Locate every blood parasite and identify its species.
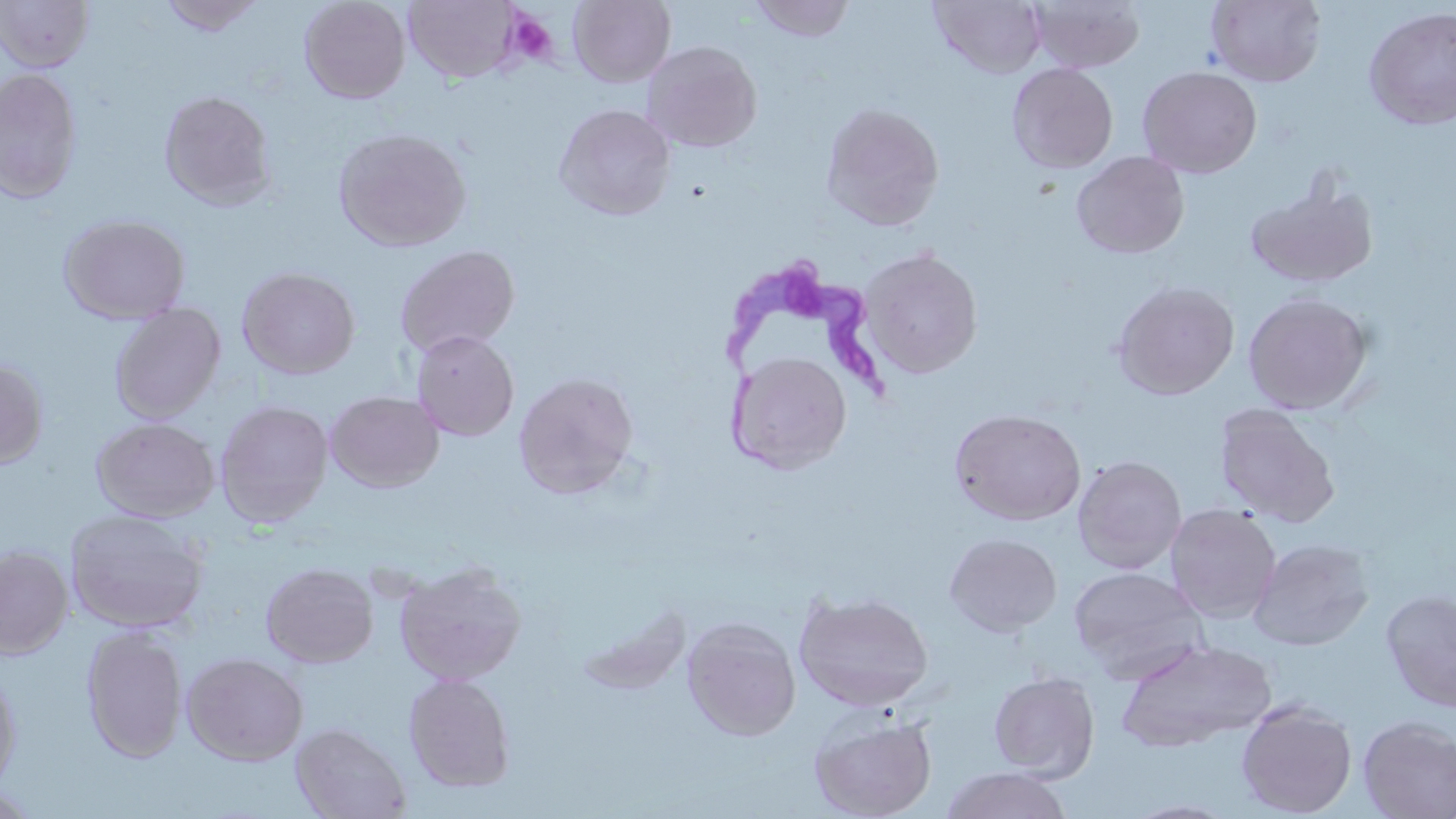

Approximate bounding boxes as (x1,y1)-(x2,y2) corner pairs in pixels.
Trypanosoma brucei: (723,255)-(890,478).
No Plasmodium falciparum, Plasmodium ovale, Plasmodium malariae, Plasmodium vivax, or Babesia divergens observed.

Platelet locations: (515,15)-(560,68). Uninfected red blood cell locations: (0,0)-(94,72), (157,0)-(267,37), (299,0)-(410,104), (568,0)-(675,87), (747,0)-(855,42), (1206,0)-(1326,87), (403,1)-(521,83), (929,1)-(1046,78), (1028,1)-(1145,74), (1363,6)-(1456,129), (642,40)-(763,153), (1007,63)-(1118,174), (1137,66)-(1262,178), (0,68)-(82,204), (158,90)-(277,209), (553,103)-(676,221), (821,103)-(944,231), (334,127)-(471,252), (1071,150)-(1190,259), (1244,177)-(1379,288), (58,213)-(192,325), (395,244)-(520,358), (859,247)-(983,378), (236,266)-(361,380), (1112,280)-(1240,399), (1243,291)-(1373,414), (109,303)-(226,424), (410,330)-(519,442), (728,351)-(852,474), (0,356)-(48,470), (513,372)-(639,499), (324,390)-(444,493), (215,400)-(334,528), (1214,404)-(1340,526), (949,409)-(1086,525), (91,417)-(220,522), (1072,454)-(1188,575), (1165,503)-(1282,623), (65,508)-(208,634), (945,533)-(1062,636), (1249,537)-(1375,651), (0,545)-(74,658), (394,560)-(527,686), (261,562)-(378,668), (1069,566)-(1208,680), (1380,588)-(1456,714), (794,589)-(934,711), (681,616)-(802,741), (81,625)-(188,762), (1114,638)-(1278,752), (181,651)-(309,765), (0,664)-(22,795), (988,670)-(1099,781), (403,672)-(516,793), (1236,699)-(1358,817), (809,711)-(937,819), (1357,716)-(1456,819), (290,721)-(412,819), (940,767)-(1073,819), (0,785)-(43,819). Slide-level diagnosis: Trypanosoma brucei. Thin blood smear. Captured at 1000x magnification. May-Grünwald-Giemsa stain. Light microscopy. Single field of view. Image is 1456×819 pixels.